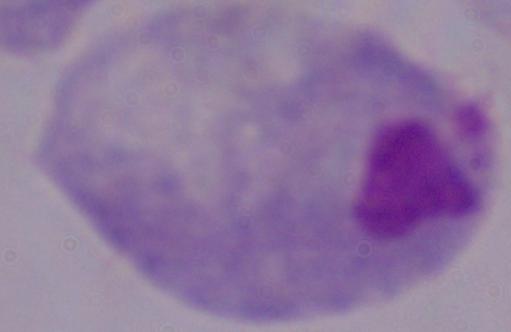

{
  "identification": "trichomonad",
  "magnification": "1000x",
  "modality": "photomicrograph"
}